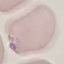

result = malaria parasites detected
stain = Giemsa
capture = smartphone through the microscope eyepiece
preparation = thin blood film
image type = cell patch, automatically extracted from a larger field of view and resized to 64 × 64 pixels